State which parasite is depicted.
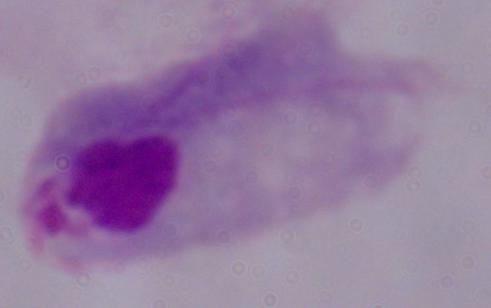
A trichomonad.

{
  "magnification": "1000x",
  "modality": "photomicrograph"
}